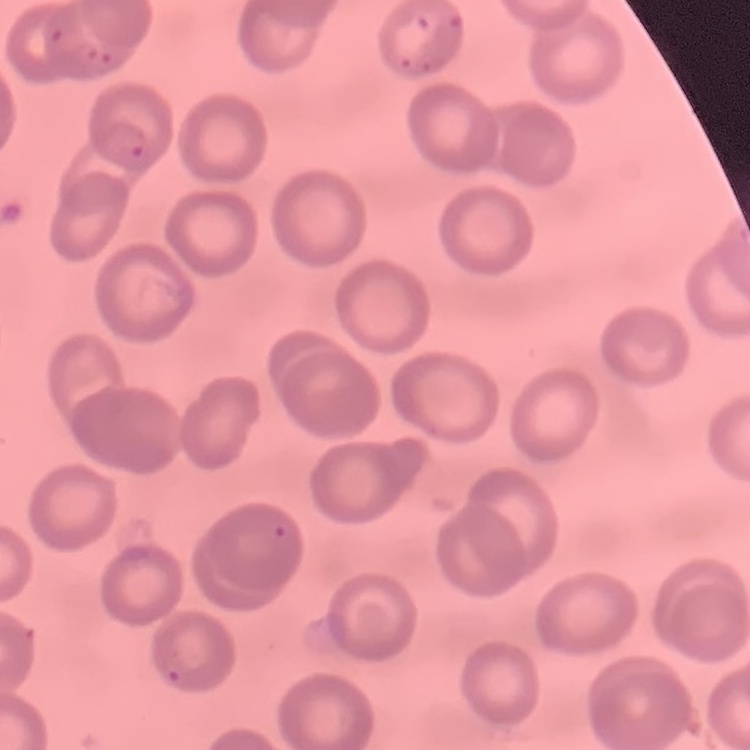
The red blood cells exhibit no rouleaux formation. Square crop of a larger photomicrograph. Thin peripheral smear. Stained with either Field's or Giemsa.